Classify this cell by malaria status.
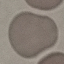

Uninfected.

stain: Giemsa
capture: smartphone camera at the microscope eyepiece
preparation: thin smear
image_type: automatically extracted cell patch, resized to 64 × 64 pixels